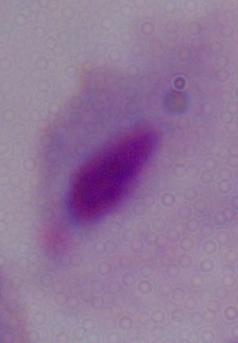
Summary:
  - Modality: photomicrograph
  - Identification: trichomonad
  - Magnification: 1000x